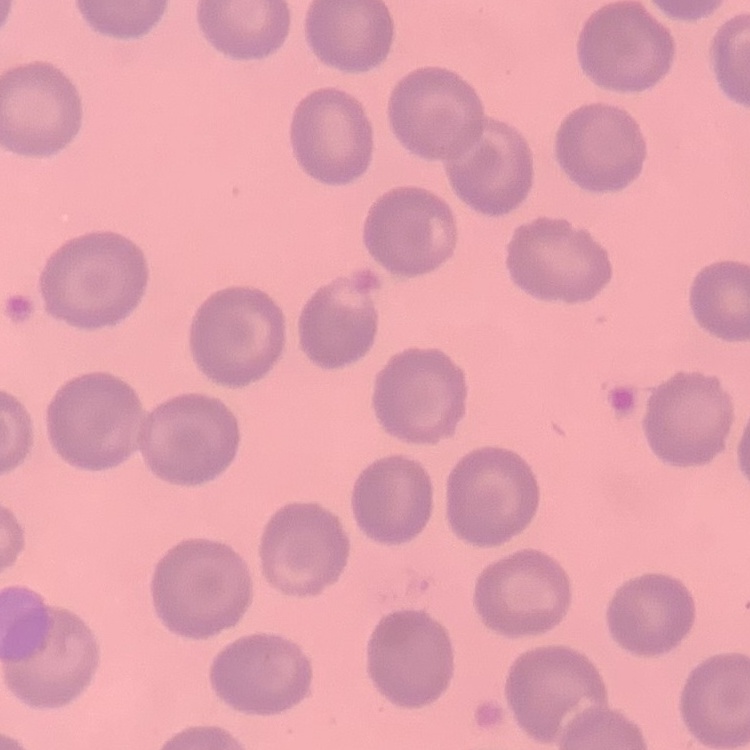
The erythrocytes show no rouleaux formation. Thin blood film. One tile cut from a larger photomicrograph. Stained with either Field's or Giemsa.